State the blood parasite species.
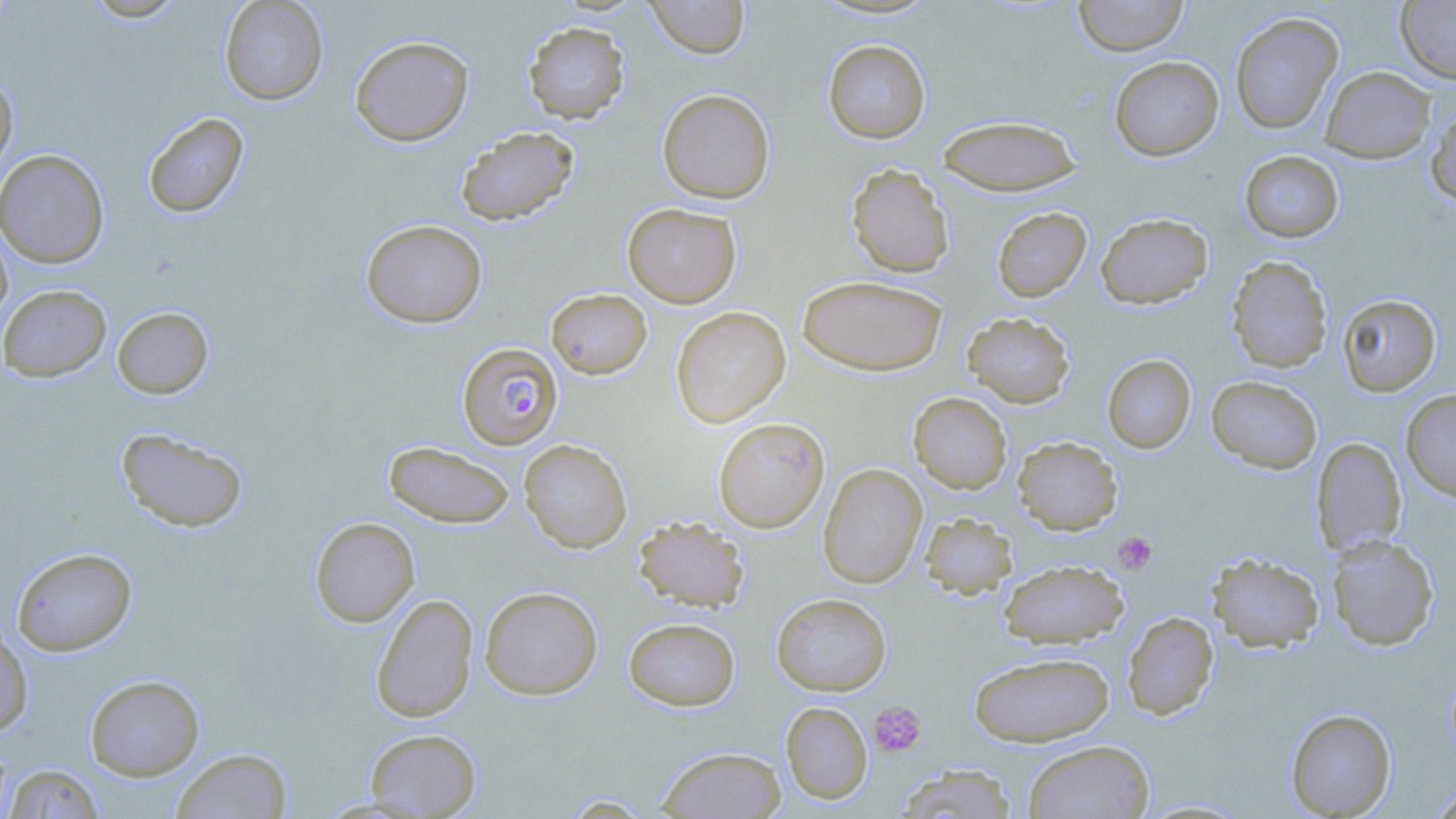
Plasmodium falciparum.

Summary:
  - Coordinate format: approximate bounding boxes as [x1, y1, x2, y2] in pixels
  - Platelet locations: [1113, 531, 1157, 575], [869, 701, 926, 757]
  - Uninfected red blood cell locations: [83, 0, 188, 22], [643, 0, 750, 58], [1073, 0, 1188, 57], [219, 1, 329, 105], [1395, 1, 1456, 83], [1229, 12, 1343, 133], [522, 21, 630, 124], [350, 35, 474, 146], [823, 39, 930, 143], [1109, 56, 1223, 161], [1320, 66, 1436, 162], [0, 71, 18, 179], [657, 89, 775, 204], [1426, 105, 1456, 206], [142, 112, 249, 218], [937, 114, 1082, 196], [455, 126, 579, 225], [0, 149, 109, 268], [1240, 150, 1344, 243], [846, 163, 954, 278], [622, 203, 741, 308], [992, 207, 1091, 302], [1096, 212, 1213, 309], [360, 219, 487, 328], [0, 224, 13, 325], [1226, 256, 1332, 373], [797, 275, 947, 376], [0, 284, 111, 382], [545, 288, 652, 380], [1337, 293, 1441, 397], [112, 306, 214, 398], [670, 306, 790, 427], [962, 312, 1074, 408], [1102, 354, 1196, 454], [1206, 375, 1322, 474], [1401, 389, 1456, 503], [908, 392, 1012, 494], [713, 417, 829, 532], [116, 427, 248, 533], [1013, 436, 1122, 535], [1311, 438, 1406, 558], [519, 439, 632, 553], [383, 440, 515, 529], [817, 463, 927, 588], [919, 512, 1017, 599], [310, 516, 420, 626], [633, 516, 750, 612], [1327, 535, 1440, 651], [11, 547, 136, 656], [1207, 552, 1325, 652], [998, 559, 1129, 648], [480, 586, 602, 699], [371, 593, 478, 722], [771, 593, 891, 695], [1123, 611, 1219, 719], [624, 617, 740, 711], [0, 623, 34, 737], [969, 651, 1114, 746], [85, 674, 205, 781], [781, 701, 873, 804], [1285, 708, 1396, 818], [364, 728, 481, 817], [1023, 740, 1155, 819], [657, 746, 786, 818], [171, 748, 292, 819], [895, 763, 1018, 818], [4, 764, 105, 818], [1425, 784, 1456, 818], [559, 794, 656, 817]
  - Plasmodium falciparum-infected red blood cell locations: [457, 343, 562, 449]
  - Magnification: 1000x
  - Preparation: thin blood film
  - Modality: optical microscopy
  - Field of view: single
  - Image size: 1456×819 pixels
  - Stain: May-Grünwald-Giemsa